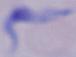 A trypanosome is shown. Photomicrograph. 1000x magnification.